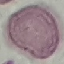
Summary:
  - Malaria status: uninfected
  - Stain: Giemsa
  - Capture: smartphone camera at the microscope eyepiece
  - Image type: automatically extracted cell patch, resized to 64 × 64 pixels
  - Preparation: thin blood film